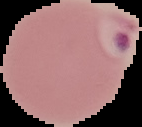 Image is 142×127 pixels. The area outside the segmented cell region is set to black. From a thin blood film. Malaria status: parasitized.